Assess this cell for malaria.
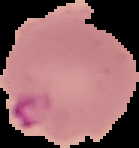

It is parasitized.

{
  "image_size": "139×148 pixels",
  "preparation": "thin blood film",
  "image_type": "cell region segmented out of the field of view; surrounding area masked to black"
}